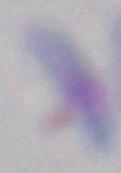 Micrograph. Toxoplasma gondii is shown. 1000x magnification.